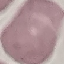

Summary:
  - Malaria status: uninfected
  - Stain: Giemsa
  - Capture: smartphone camera at the microscope eyepiece
  - Image type: automatically extracted cell patch, resized to 64 × 64 pixels
  - Preparation: thin blood film